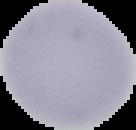
Summary:
  - Image type: cell region segmented out of the field of view; surrounding area masked to black
  - Result: no malaria parasites seen
  - Image size: 136×130 pixels
  - Preparation: thin blood smear